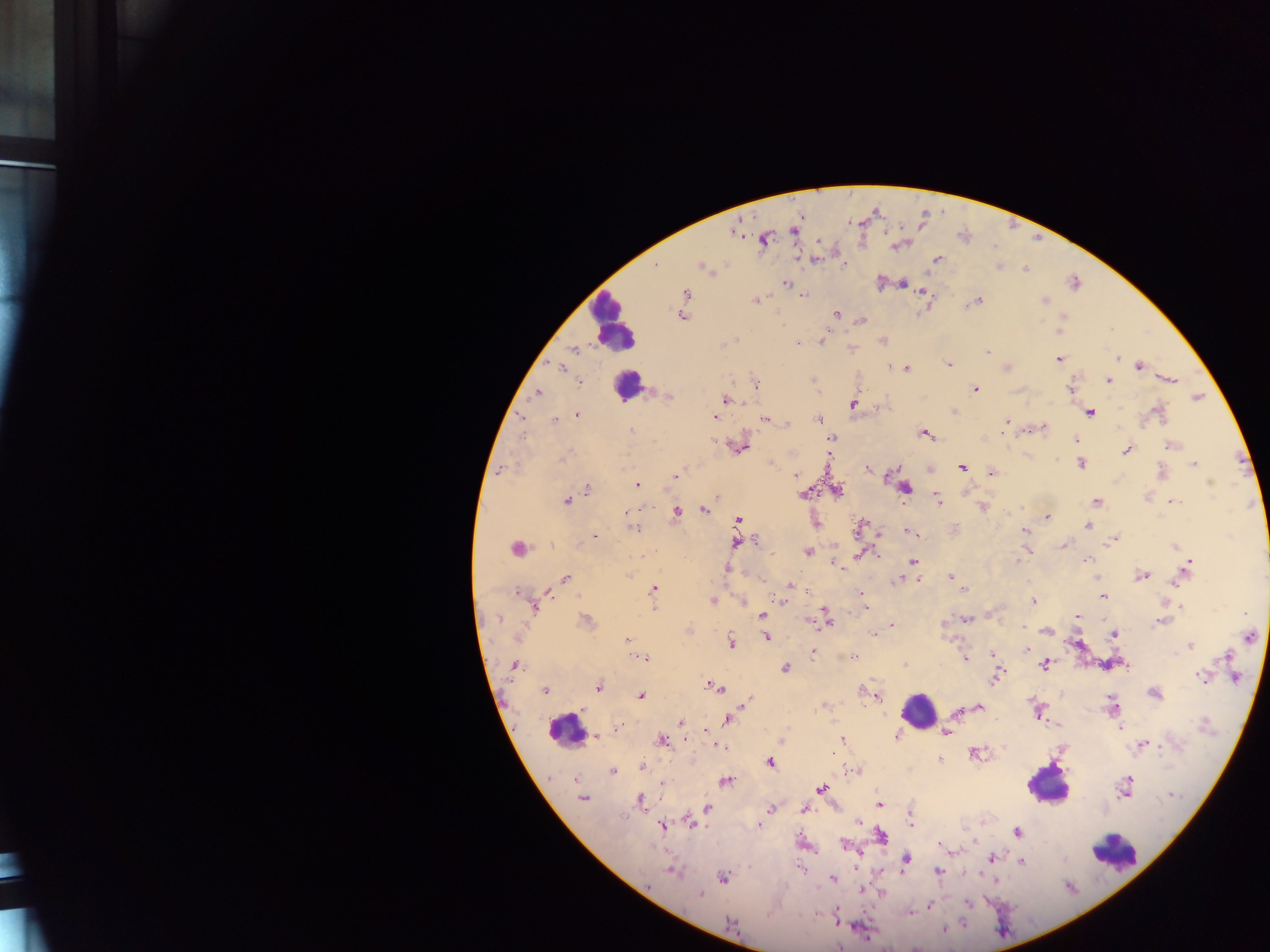
Approximate centers as {x, y} in pixels. Leukocyte locations: {611, 324}, {627, 385}, {918, 711}, {565, 727}, {1047, 784}, {1114, 850}. Plasmodium parasite locations: {793, 230}, {733, 231}, {764, 240}, {897, 246}, {815, 259}, {937, 260}, {843, 265}, {999, 267}, {704, 269}, {1025, 269}, {786, 283}, {903, 283}, {1075, 283}, {685, 293}, {923, 293}, {802, 295}, {1045, 300}, {755, 301}, {976, 301}, {970, 304}, {836, 314}, {682, 317}, {862, 319}, {1059, 331}, {734, 340}, {821, 341}, {883, 341}, {796, 343}, {852, 348}, {575, 349}, {987, 350}, {1058, 359}, {1117, 359}, {949, 364}, {1140, 366}, {560, 367}, {891, 367}, {907, 368}, {1006, 368}, {812, 379}, {1171, 380}, {1108, 381}, {580, 382}, {757, 384}, {1070, 388}, {975, 389}, {537, 393}, {669, 397}, {1197, 397}, {726, 399}, {852, 404}, {955, 412}, {1090, 412}, {1157, 412}, {577, 414}, {522, 417}, {714, 417}, {766, 419}, {819, 419}, {554, 421}, {1006, 422}, {786, 423}, {1005, 428}, {1043, 428}, {630, 430}, {925, 433}, {1003, 433}, {521, 436}, {831, 438}, {1075, 440}, {1172, 445}, {740, 448}, {1126, 450}, {564, 458}, {1080, 463}, {1194, 464}, {961, 467}, {501, 469}, {867, 469}, {1161, 472}, {991, 474}, {795, 475}, {676, 476}, {1211, 483}, {637, 485}, {588, 488}, {905, 488}, {838, 491}, {803, 494}, {716, 497}, {937, 498}, {567, 500}, {1096, 501}, {1172, 501}, {982, 508}, {703, 510}, {676, 511}, {626, 512}, {1047, 517}, {738, 519}, {860, 526}, {1088, 526}, {634, 527}, {955, 527}, {1025, 531}, {910, 532}, {595, 536}, {1114, 538}, {757, 541}, {736, 543}, {1063, 546}, {1175, 546}, {516, 549}, {1027, 550}, {807, 552}, {862, 554}, {641, 556}, {1086, 560}, {913, 561}, {1017, 562}, {835, 563}, {1189, 565}, {726, 569}, {629, 575}, {1141, 576}, {950, 577}, {566, 578}, {901, 578}, {917, 579}, {1176, 581}, {790, 585}, {653, 589}, {965, 589}, {548, 591}, {517, 592}, {861, 593}, {1103, 596}, {712, 601}, {781, 601}, {743, 602}, {1034, 602}, {653, 606}, {1182, 606}, {534, 608}, {866, 608}, {762, 615}, {1078, 617}, {498, 618}, {967, 620}, {586, 621}, {826, 621}, {1160, 622}, {892, 625}, {1022, 627}, {688, 631}, {1047, 631}, {873, 635}, {1113, 635}, {1250, 637}, {766, 638}, {627, 640}, {732, 642}, {1190, 645}, {1027, 650}, {813, 652}, {992, 653}, {853, 656}, {1226, 657}, {643, 659}, {965, 659}, {1044, 665}, {514, 666}, {1125, 666}, {785, 668}, {996, 676}, {1200, 676}, {1235, 678}, {597, 687}, {716, 687}, {862, 689}, {545, 690}, {1154, 693}, {641, 696}, {877, 696}, {748, 700}, {746, 703}, {979, 706}, {1113, 706}, {584, 710}, {956, 712}, {1038, 712}, {726, 719}, {681, 722}, {1204, 725}, {1121, 728}, {615, 730}, {705, 730}, {946, 733}, {896, 734}, {595, 736}, {842, 739}, {686, 740}, {661, 741}, {781, 742}, {1142, 745}, {720, 746}, {974, 753}, {940, 760}, {770, 763}, {642, 767}, {612, 771}, {856, 771}, {726, 781}, {663, 783}, {822, 788}, {1125, 790}, {1171, 796}, {582, 798}, {641, 801}, {879, 804}, {708, 809}, {771, 809}, {804, 809}, {859, 822}, {691, 823}, {911, 824}, {662, 826}, {759, 826}, {1016, 832}, {881, 835}, {844, 845}, {941, 845}, {992, 858}, {905, 859}, {1022, 862}, {801, 870}, {937, 872}, {673, 873}, {723, 878}, {833, 879}, {995, 880}, {862, 890}, {700, 895}, {967, 904}, {929, 906}, {911, 913}, {730, 923}, {944, 929}, {839, 947}. Single field of view. Image is 1270×952 pixels. Thick blood film. Mobile-phone photograph taken through the microscope. Sample from Ghana.